Classify this cell by malaria status.
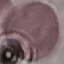
Uninfected.

Thin blood film. Automatically extracted cell patch, resized to 64 × 64 pixels. Acquired by smartphone through the microscope eyepiece. Giemsa stain.